Describe the morphology of the erythrocytes.
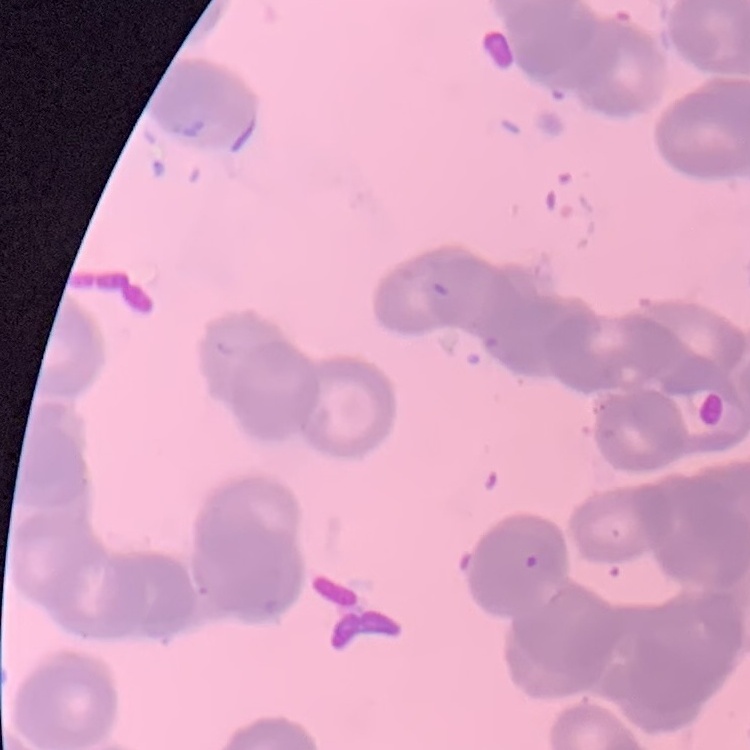

They show rouleaux formation.

image_type: one tile cut from a larger photomicrograph
stain: Field's or Giemsa
preparation: thin blood smear